Identify the cell.
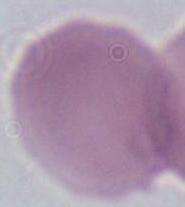
An erythrocyte.

Summary:
  - Modality: micrograph
  - Magnification: 1000x